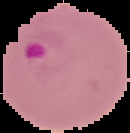
Result: Plasmodium parasites identified. Cell region segmented out of the field of view; the surrounding area is masked to black. Image is 130×133 pixels. From a thin blood film.